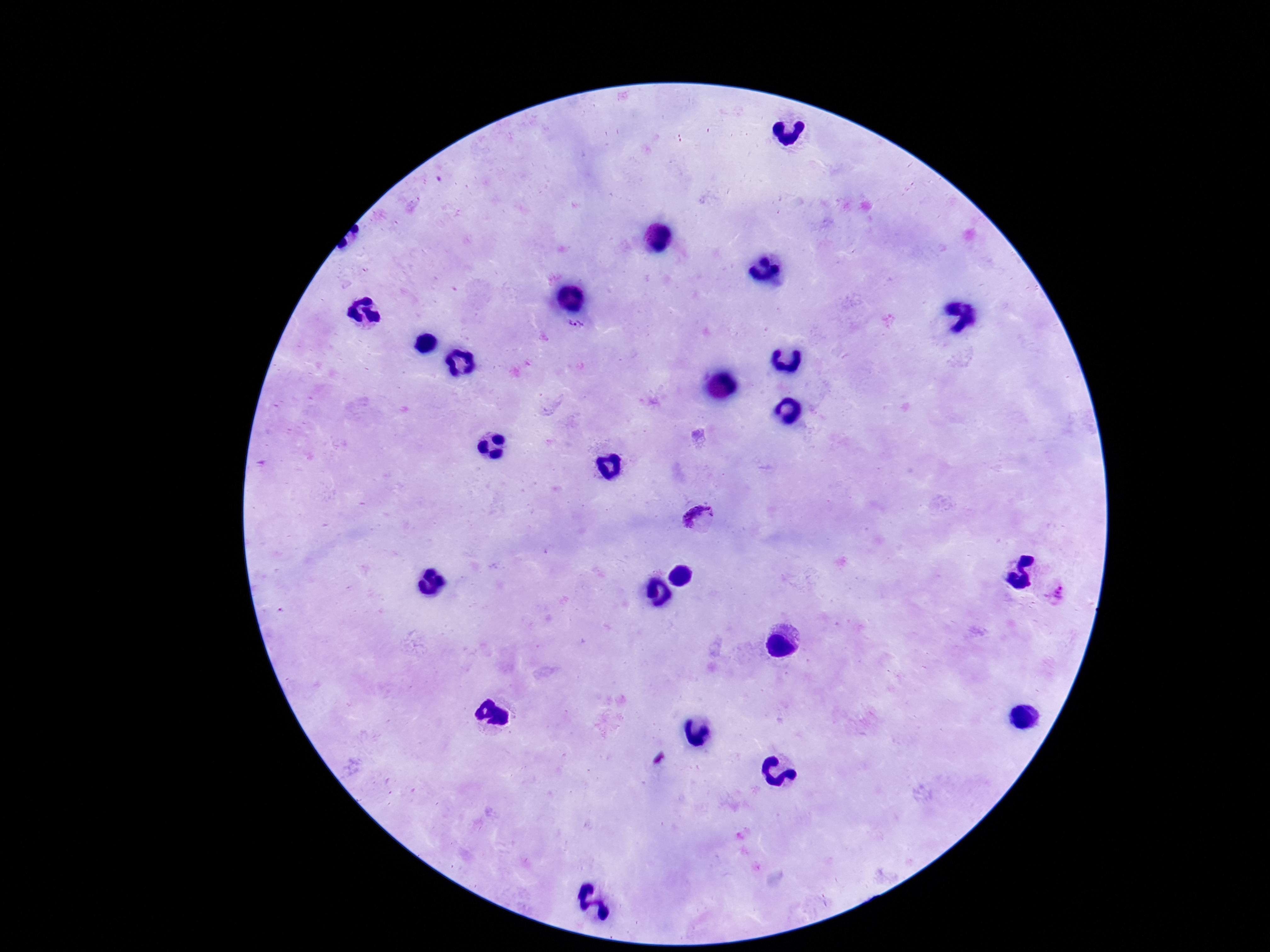
Approximate centers as {x, y} in pixels.
Summary:
  - Plasmodium parasite locations: {578, 330}, {699, 521}, {1055, 591}
  - Field of view: one from this slide
  - Preparation: thick blood smear
  - Stain: Giemsa
  - Image size: 1270×952 pixels
  - Patient malaria status: positive
  - Capture: smartphone camera through the microscope eyepiece
  - Magnification: 100x